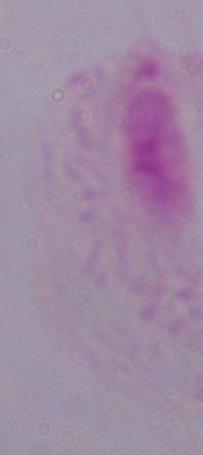 1000x magnification. A trichomonad is shown. Micrograph.